Locate every blood parasite and identify its species.
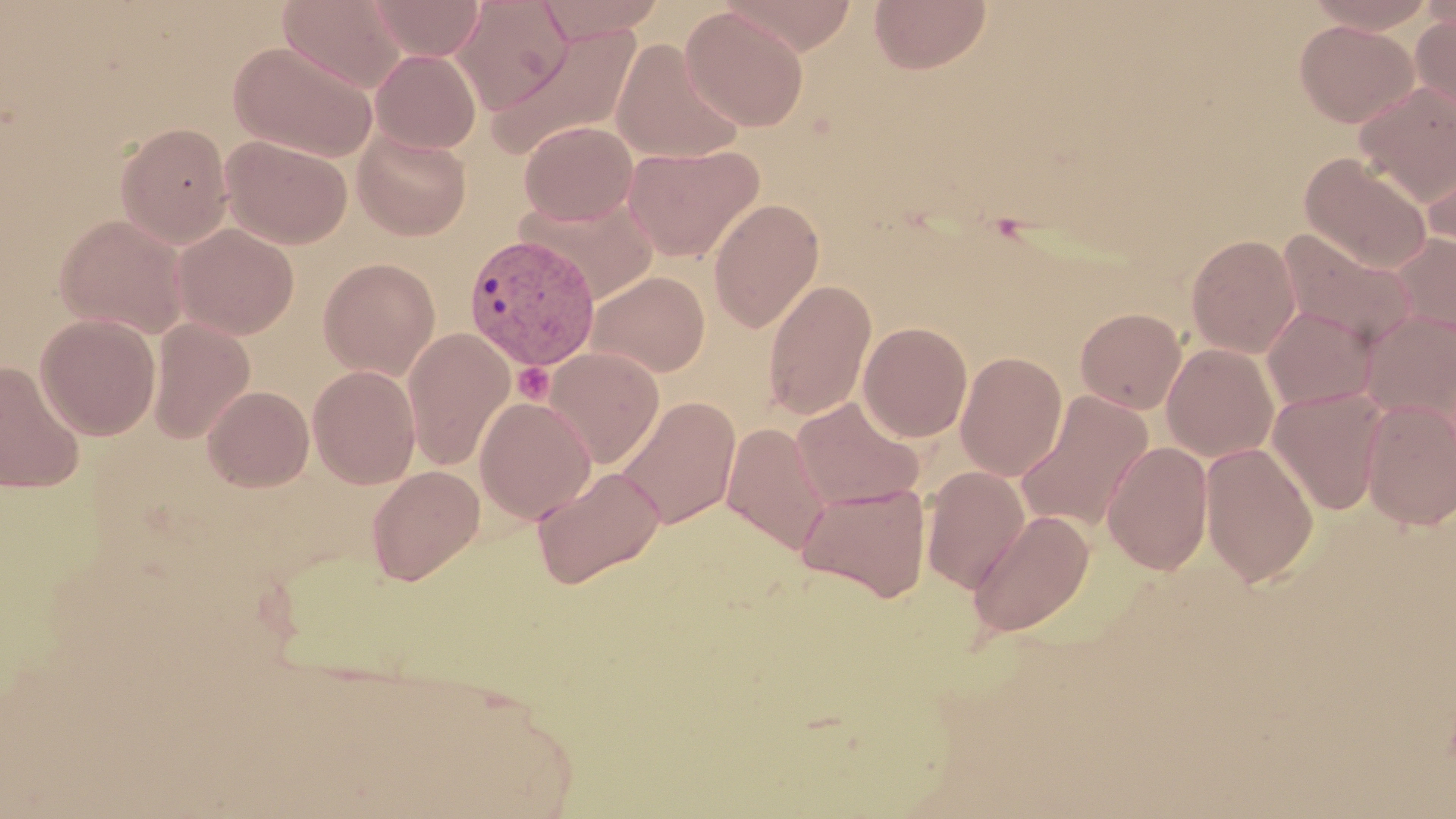
Approximate bounding boxes as named x1/y1/x2/y2 corners in pixels.
Plasmodium vivax-infected red blood cells: (x1=462, y1=233, x2=601, y2=372).
No Plasmodium falciparum, Plasmodium ovale, Plasmodium malariae, Babesia divergens, or Trypanosoma brucei observed.

Uninfected red blood cell locations: (x1=278, y1=0, x2=407, y2=93), (x1=367, y1=0, x2=485, y2=61), (x1=451, y1=0, x2=573, y2=113), (x1=535, y1=0, x2=664, y2=43), (x1=722, y1=0, x2=859, y2=54), (x1=869, y1=0, x2=992, y2=74), (x1=1303, y1=0, x2=1439, y2=33), (x1=681, y1=6, x2=809, y2=131), (x1=1411, y1=12, x2=1456, y2=117), (x1=1294, y1=19, x2=1419, y2=127), (x1=487, y1=24, x2=642, y2=160), (x1=610, y1=39, x2=744, y2=164), (x1=229, y1=40, x2=378, y2=161), (x1=370, y1=49, x2=482, y2=154), (x1=1355, y1=82, x2=1456, y2=204), (x1=519, y1=120, x2=638, y2=226), (x1=116, y1=122, x2=233, y2=248), (x1=353, y1=131, x2=472, y2=241), (x1=220, y1=135, x2=353, y2=249), (x1=623, y1=143, x2=764, y2=262), (x1=1421, y1=145, x2=1456, y2=259), (x1=1299, y1=152, x2=1433, y2=273), (x1=519, y1=191, x2=659, y2=303), (x1=708, y1=197, x2=825, y2=333), (x1=54, y1=214, x2=190, y2=339), (x1=172, y1=223, x2=299, y2=340), (x1=1278, y1=228, x2=1418, y2=347), (x1=1388, y1=233, x2=1456, y2=340), (x1=1186, y1=234, x2=1302, y2=357), (x1=318, y1=257, x2=440, y2=379), (x1=587, y1=270, x2=711, y2=378), (x1=762, y1=279, x2=876, y2=421), (x1=1262, y1=305, x2=1379, y2=412), (x1=1075, y1=307, x2=1187, y2=414), (x1=1360, y1=310, x2=1456, y2=425), (x1=35, y1=313, x2=161, y2=440), (x1=147, y1=317, x2=255, y2=443), (x1=859, y1=322, x2=973, y2=441), (x1=402, y1=328, x2=515, y2=471), (x1=1161, y1=343, x2=1279, y2=462), (x1=543, y1=346, x2=664, y2=469), (x1=955, y1=351, x2=1068, y2=480), (x1=0, y1=360, x2=86, y2=495), (x1=308, y1=365, x2=420, y2=489), (x1=203, y1=385, x2=314, y2=492), (x1=1267, y1=388, x2=1388, y2=515), (x1=1015, y1=391, x2=1154, y2=533), (x1=616, y1=395, x2=741, y2=530), (x1=475, y1=396, x2=596, y2=524), (x1=791, y1=398, x2=924, y2=512), (x1=1360, y1=398, x2=1456, y2=530), (x1=720, y1=422, x2=831, y2=554), (x1=1101, y1=440, x2=1214, y2=574), (x1=1199, y1=442, x2=1319, y2=586), (x1=366, y1=464, x2=484, y2=585), (x1=533, y1=466, x2=665, y2=588), (x1=920, y1=467, x2=1030, y2=593), (x1=796, y1=480, x2=931, y2=603), (x1=967, y1=509, x2=1095, y2=637). Platelet locations: (x1=512, y1=362, x2=554, y2=404). Slide-level diagnosis: Plasmodium vivax. Image is 1456×819 pixels. May-Grünwald-Giemsa stain. Light microscopy. One field of a larger specimen. Thin blood smear. Captured at 1000x magnification.